Identify the preparation type.
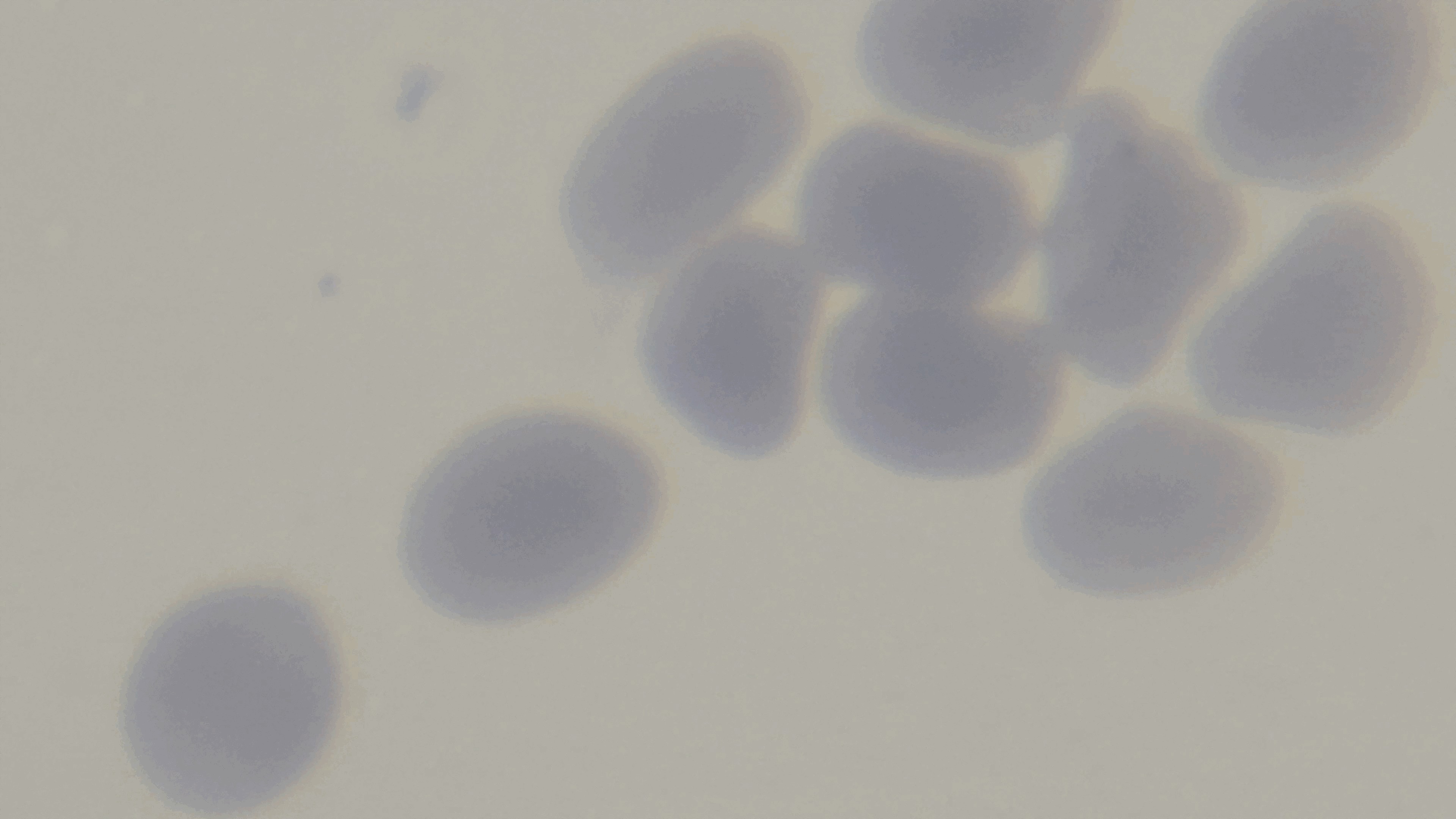

A thin smear.

Summary:
  - Objective: 100x oil immersion
  - Capture: mounted 4K digital camera
  - Stain: Giemsa
  - Malaria status: negative
  - Modality: light microscopy
  - Field of view: one from the slide